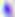 Photomicrograph. Captured at 400x magnification. Toxoplasma gondii is seen.